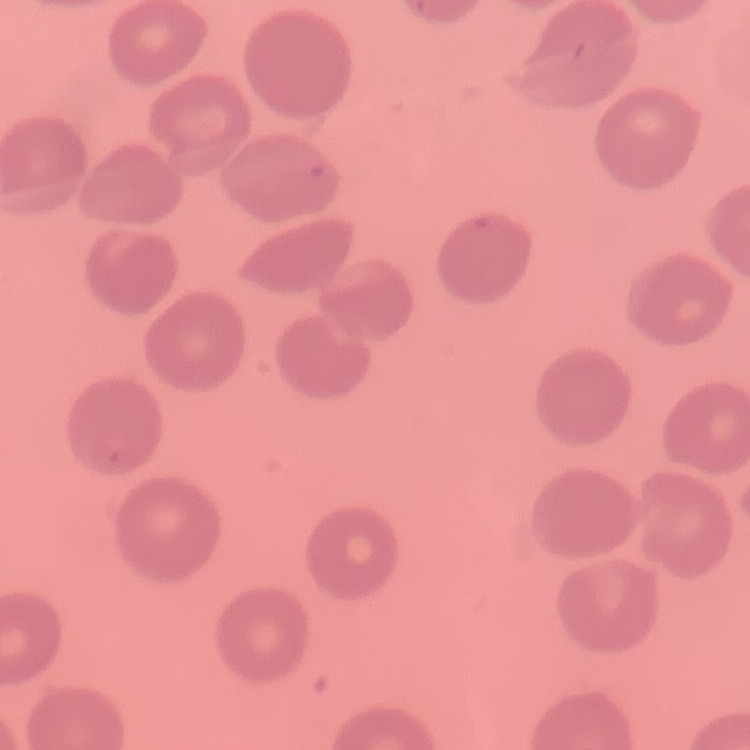

erythrocyte morphology = no rouleaux formation
stain = Field's or Giemsa
preparation = thin blood smear
image type = one tile cut from a larger photomicrograph